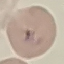

Summary:
  - Malaria status: uninfected
  - Capture: smartphone through the microscope eyepiece
  - Image type: automatically extracted cell patch, resized to 64 × 64 pixels
  - Stain: Giemsa
  - Preparation: thin smear